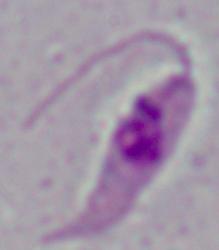

{
  "magnification": "1000x",
  "modality": "micrograph",
  "identification": "Leishmania"
}